State the preparation type.
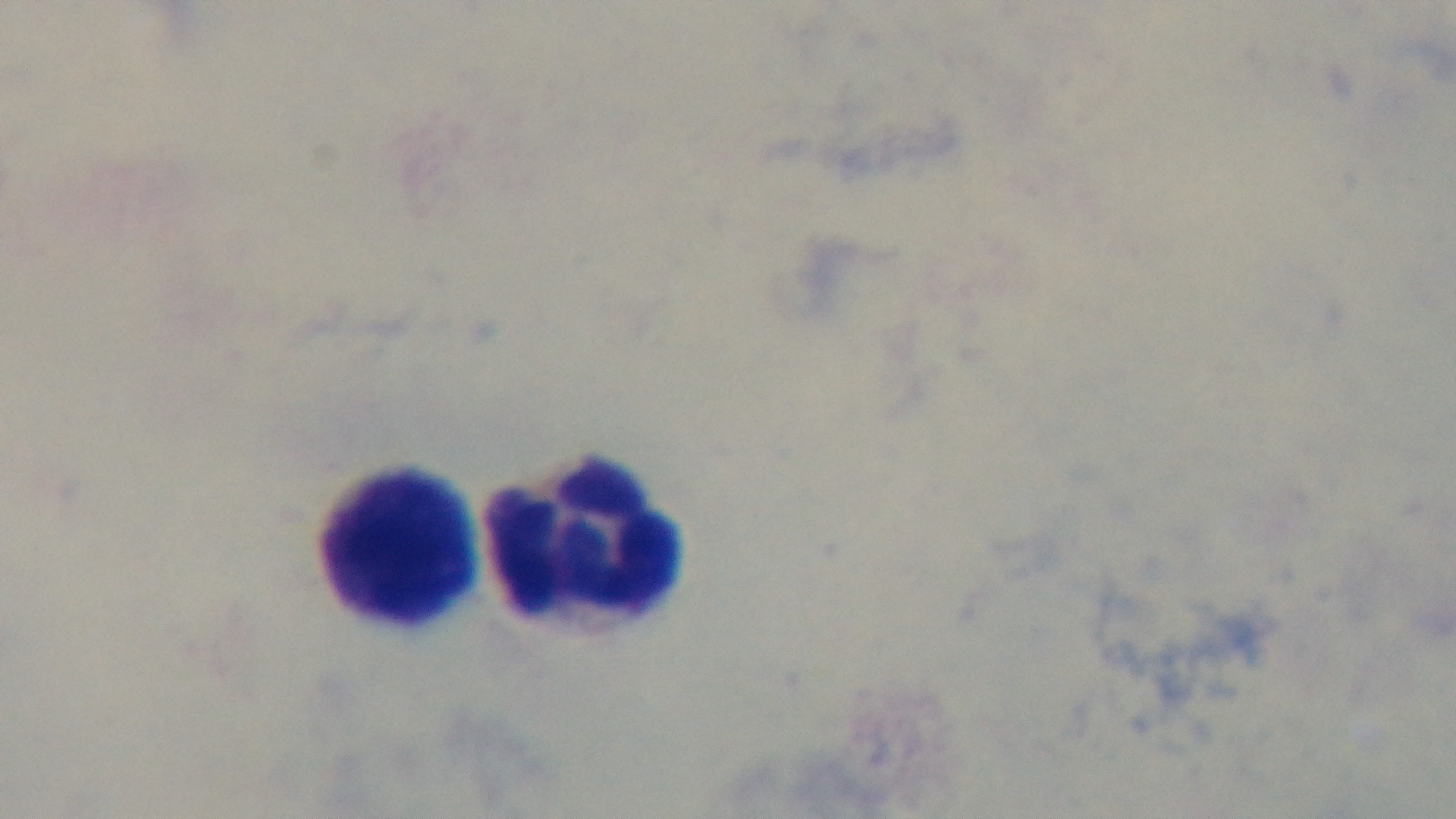

A thick smear.

field of view = single
malaria status = negative
stain = Giemsa
modality = light microscopy
capture = mounted 4K digital camera
objective = 100x oil immersion